Identify the parasite.
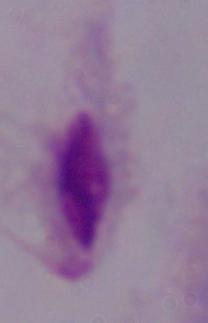
A trichomonad.

magnification = 1000x
modality = photomicrograph